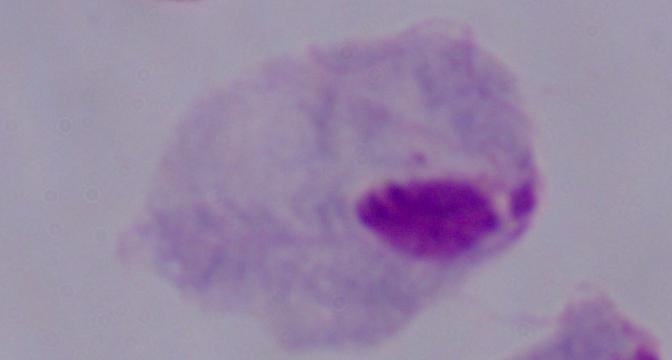

Micrograph. A trichomonad is seen. Captured at 1000x magnification.